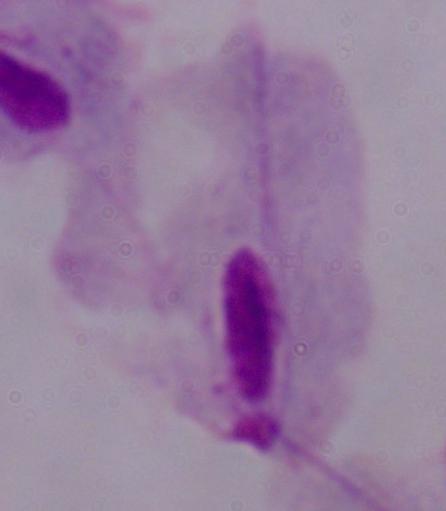

Summary:
  - Identification: trichomonad
  - Modality: photomicrograph
  - Magnification: 1000x